Locate every blood parasite and identify its species.
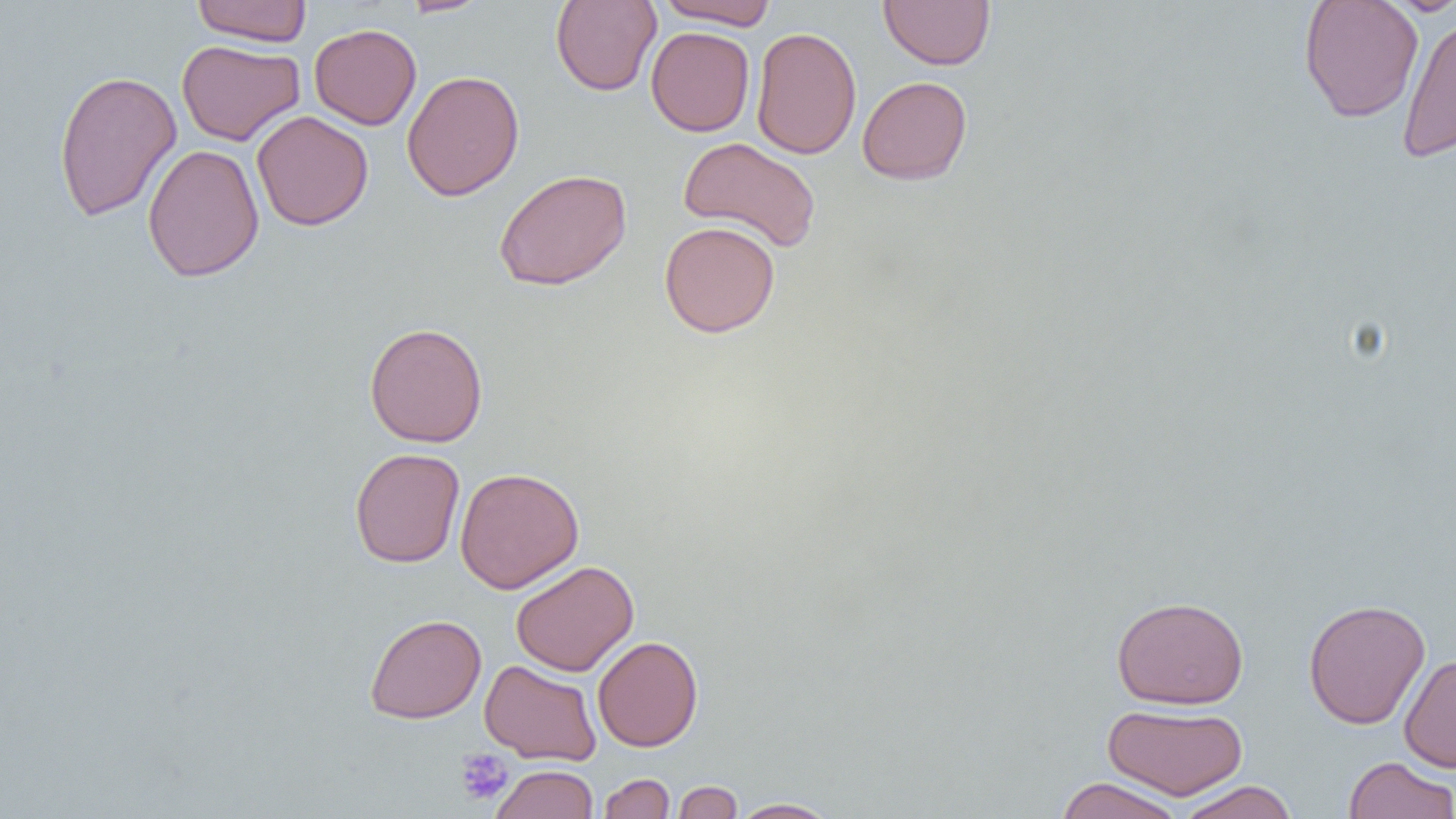

No blood parasites observed.

{
  "slide_level_diagnosis": "no evidence of blood parasites",
  "preparation": "thin blood film",
  "magnification": "1000x",
  "uninfected_red_blood_cell_locations": "approximate bounding boxes as named x1/y1/x2/y2 corners in pixels: (x1=191, y1=0, x2=312, y2=46), (x1=398, y1=0, x2=493, y2=17), (x1=654, y1=0, x2=779, y2=29), (x1=879, y1=0, x2=995, y2=70), (x1=550, y1=1, x2=662, y2=96), (x1=1298, y1=1, x2=1424, y2=123), (x1=1396, y1=11, x2=1456, y2=164), (x1=309, y1=23, x2=421, y2=130), (x1=751, y1=26, x2=862, y2=159), (x1=646, y1=27, x2=755, y2=136), (x1=177, y1=39, x2=305, y2=146), (x1=53, y1=69, x2=182, y2=222), (x1=402, y1=70, x2=524, y2=201), (x1=857, y1=75, x2=972, y2=185), (x1=251, y1=110, x2=373, y2=231), (x1=678, y1=137, x2=822, y2=254), (x1=142, y1=143, x2=265, y2=282), (x1=493, y1=168, x2=632, y2=291), (x1=659, y1=221, x2=780, y2=338), (x1=364, y1=322, x2=489, y2=448), (x1=350, y1=448, x2=465, y2=568), (x1=454, y1=466, x2=584, y2=594), (x1=510, y1=560, x2=639, y2=677), (x1=1111, y1=595, x2=1249, y2=709), (x1=1303, y1=599, x2=1431, y2=729), (x1=364, y1=613, x2=487, y2=724), (x1=592, y1=636, x2=703, y2=751), (x1=1399, y1=653, x2=1456, y2=773), (x1=479, y1=659, x2=602, y2=766), (x1=1103, y1=703, x2=1248, y2=800), (x1=1343, y1=756, x2=1455, y2=819), (x1=490, y1=764, x2=599, y2=819), (x1=599, y1=773, x2=675, y2=818), (x1=1055, y1=776, x2=1186, y2=819), (x1=672, y1=779, x2=743, y2=819), (x1=1175, y1=781, x2=1299, y2=819), (x1=728, y1=797, x2=841, y2=818)",
  "platelet_locations": "approximate bounding boxes as named x1/y1/x2/y2 corners in pixels: (x1=455, y1=748, x2=514, y2=805)",
  "image_size": "1456×819 pixels",
  "modality": "optical microscopy",
  "field_of_view": "one of a larger specimen"
}